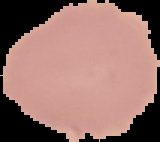
image type = segmented cell region on a black background
result = negative for malaria parasites
preparation = thin blood smear
image size = 160×142 pixels